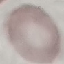
{
  "malaria_status": "uninfected",
  "preparation": "thin blood film",
  "image_type": "cell patch, automatically extracted from a larger field of view and resized to 64 × 64 pixels",
  "stain": "Giemsa",
  "capture": "smartphone through the microscope eyepiece"
}